Classify this cell by malaria status.
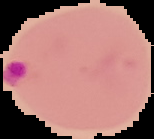
It is parasitized.

image_type: segmented cell region on a black background
preparation: thin blood film
image_size: 154×139 pixels